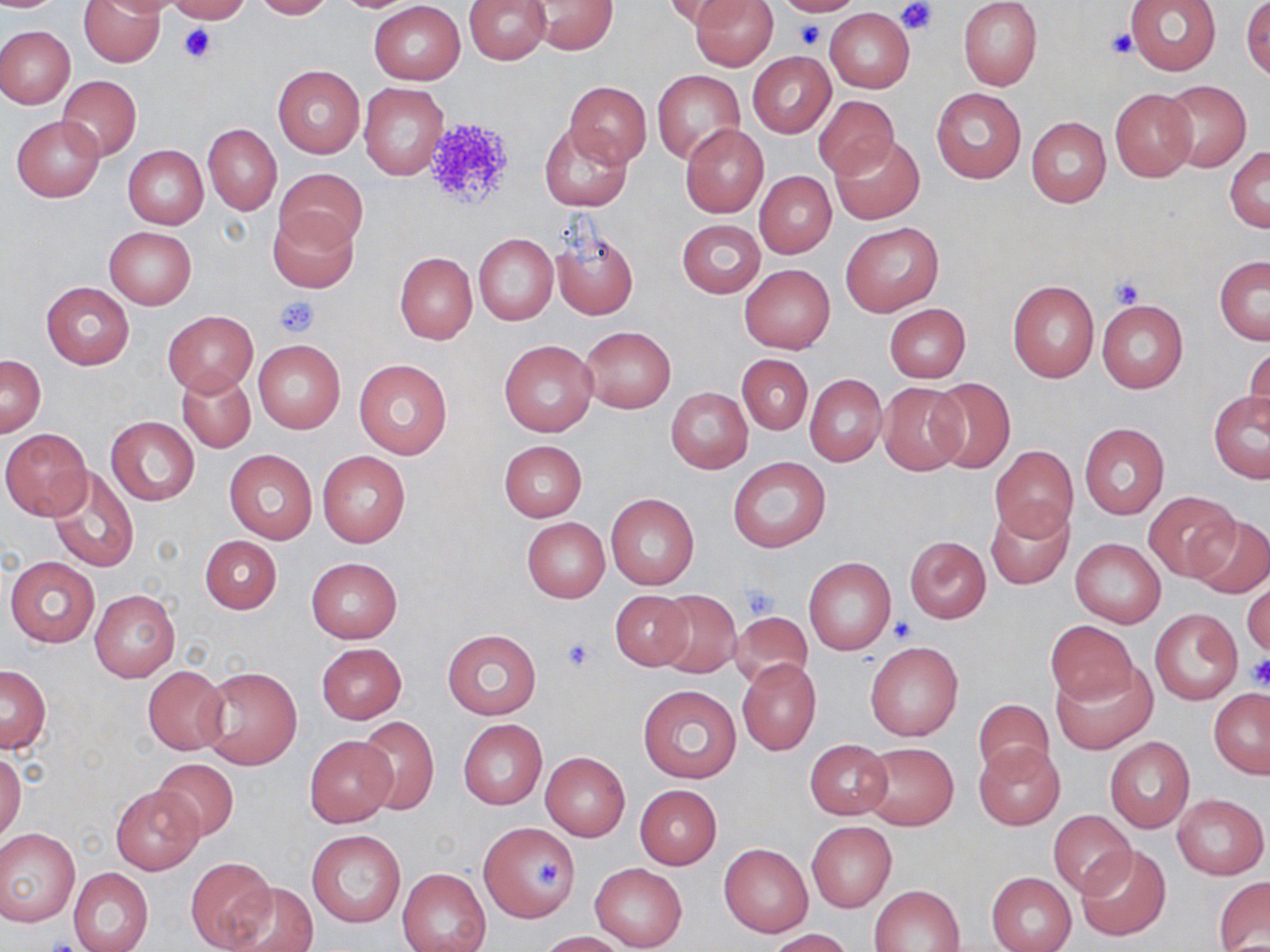
Summary:
  - Coordinate format: approximate bounding boxes as (x1,y1)-(x2,y2) corner pairs in pixels
  - Uninfected red blood cell locations: (78,0)-(165,67), (91,0)-(182,17), (167,0)-(250,23), (250,0)-(333,20), (463,0)-(552,64), (665,0)-(744,31), (691,0)-(778,70), (770,0)-(864,16), (1124,0)-(1220,75), (370,1)-(465,84), (528,1)-(617,54), (957,1)-(1043,90), (1242,1)-(1270,79), (824,9)-(914,92), (0,26)-(74,108), (747,51)-(836,137), (273,65)-(364,157), (652,70)-(746,163), (57,76)-(141,160), (1159,81)-(1253,172), (359,82)-(447,180), (564,82)-(651,167), (931,87)-(1027,183), (1110,87)-(1198,182), (814,95)-(899,180), (12,115)-(105,201), (1026,116)-(1111,207), (540,121)-(634,212), (203,123)-(282,215), (681,124)-(770,218), (832,135)-(924,224), (123,145)-(208,229), (1226,147)-(1270,232), (275,167)-(367,248), (754,171)-(837,258), (268,207)-(360,294), (677,219)-(766,297), (840,222)-(943,316), (104,227)-(195,309), (550,227)-(639,322), (473,233)-(558,325), (395,251)-(477,343), (1214,256)-(1270,344), (740,265)-(835,353), (1008,281)-(1098,381), (41,282)-(134,369), (1096,300)-(1189,393), (883,303)-(970,383), (164,311)-(257,394), (580,326)-(675,413), (498,338)-(599,437), (253,339)-(345,434), (1245,344)-(1270,433), (1,353)-(46,437), (736,353)-(813,435), (353,358)-(453,459), (178,369)-(255,452), (804,372)-(887,467), (926,377)-(1016,473), (878,383)-(966,475), (666,388)-(752,473), (1209,390)-(1270,482), (106,416)-(199,504), (1079,423)-(1169,519), (2,429)-(92,520), (498,439)-(586,522), (990,445)-(1077,539), (225,449)-(317,544), (317,451)-(411,547), (727,457)-(831,552), (48,467)-(138,573), (1144,491)-(1240,581), (605,493)-(699,589), (985,502)-(1073,588), (1189,516)-(1270,595), (521,518)-(608,602), (199,535)-(282,613), (904,536)-(992,623), (1070,537)-(1166,628), (4,557)-(99,647), (305,557)-(401,643), (804,557)-(897,656), (1243,575)-(1270,659), (89,589)-(180,683), (609,590)-(696,671), (654,590)-(741,677), (1149,607)-(1243,704), (728,611)-(813,690), (1045,620)-(1137,706), (442,628)-(542,721), (864,641)-(962,741), (316,643)-(407,724), (737,659)-(822,756), (1051,663)-(1156,754), (1,664)-(51,753), (143,665)-(229,755), (197,666)-(302,770), (638,685)-(742,784), (1209,689)-(1270,779), (973,698)-(1054,779), (354,718)-(440,815), (459,720)-(547,809), (1104,736)-(1195,832), (305,737)-(395,827), (804,739)-(892,819), (861,742)-(959,831), (974,742)-(1064,831), (540,752)-(630,840), (0,753)-(24,845), (151,758)-(240,842), (634,785)-(722,868), (111,786)-(204,874), (1171,793)-(1267,880), (1048,810)-(1135,897), (806,821)-(897,912), (479,823)-(580,923), (0,829)-(79,926), (305,830)-(406,927), (719,844)-(813,938), (1077,844)-(1170,940), (184,857)-(277,952), (590,863)-(687,950), (67,868)-(154,952), (398,868)-(490,952), (986,872)-(1077,952), (1215,877)-(1270,950), (218,879)-(318,952), (869,883)-(965,951), (767,929)-(854,952), (537,931)-(626,951)
  - Platelet locations: (897,2)-(938,38), (793,20)-(827,49), (179,24)-(215,63), (1107,28)-(1138,60), (417,115)-(518,209), (1107,274)-(1147,309), (274,295)-(319,337), (740,582)-(778,619), (890,618)-(915,643), (560,637)-(598,673), (1246,653)-(1270,691), (535,858)-(565,889)
  - Slide-level diagnosis: no evidence of blood parasites
  - Preparation: thin blood film
  - Magnification: 1000x
  - Field of view: one of a larger specimen
  - Stain: May-Grünwald-Giemsa
  - Image size: 1270×952 pixels
  - Modality: optical microscopy